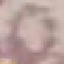

{
  "result": "no malaria parasites seen",
  "stain": "Giemsa",
  "capture": "smartphone through the microscope eyepiece",
  "preparation": "thin blood film",
  "image_type": "automatically extracted cell patch, resized to 64 × 64 pixels"
}